Give the extent of all Plasmodium falciparum-infected red blood cells.
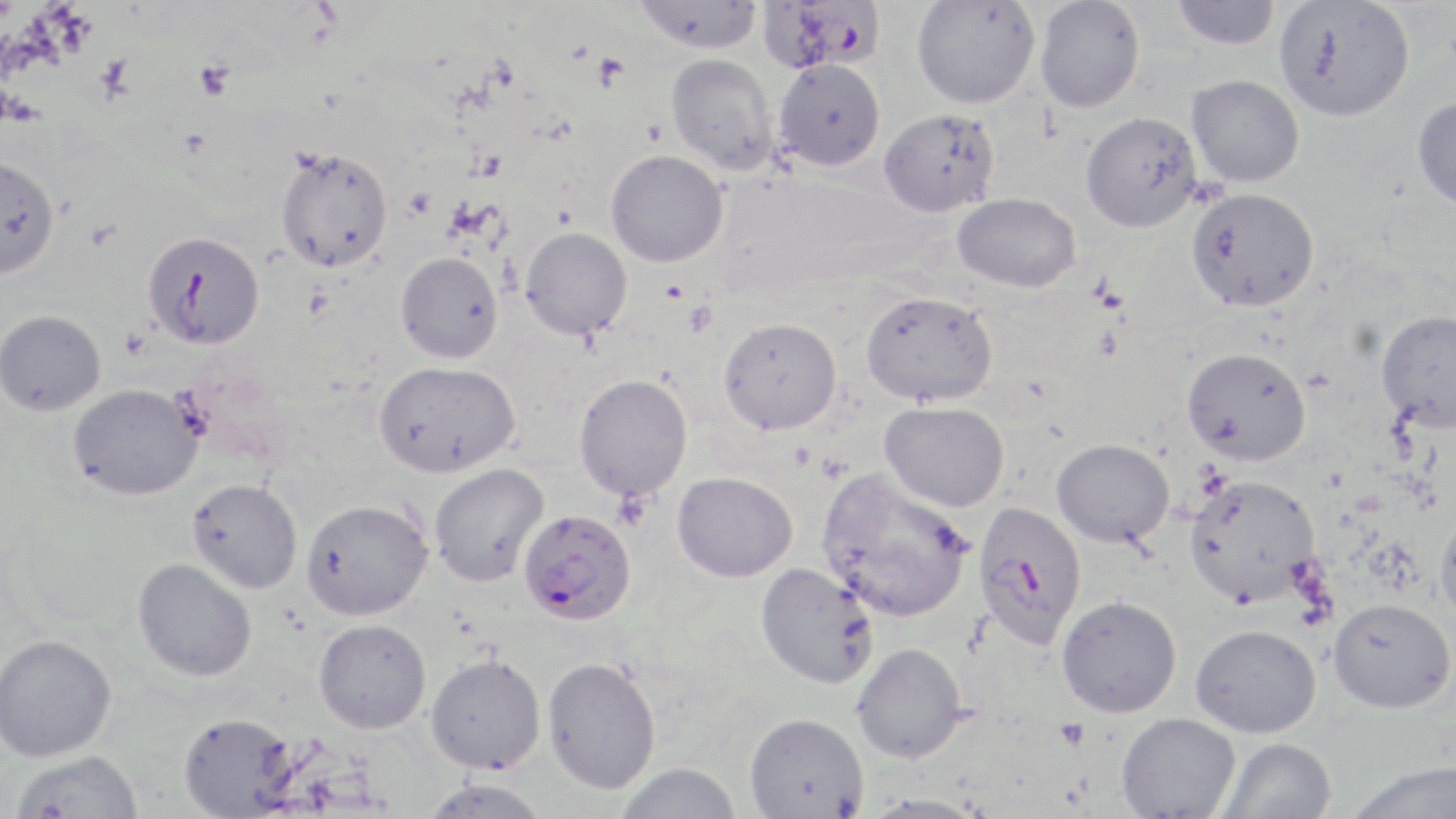
Approximate bounding boxes as [x1, y1, x2, y2] in pixels.
Plasmodium falciparum-infected red blood cells: [758, 0, 885, 74], [142, 230, 265, 349], [973, 501, 1088, 650], [518, 509, 636, 626].

Uninfected red blood cell locations: [632, 0, 765, 54], [911, 0, 1040, 109], [1035, 0, 1145, 113], [1172, 0, 1282, 50], [1274, 0, 1416, 121], [666, 53, 778, 174], [773, 59, 885, 171], [1187, 75, 1304, 188], [1412, 96, 1456, 211], [878, 109, 1000, 217], [1080, 111, 1202, 232], [275, 146, 394, 272], [605, 149, 728, 267], [0, 154, 59, 278], [1186, 187, 1319, 311], [952, 193, 1080, 292], [520, 227, 633, 340], [396, 252, 503, 364], [861, 290, 997, 407], [1375, 308, 1456, 434], [0, 310, 105, 415], [718, 317, 842, 435], [1182, 346, 1312, 465], [374, 360, 519, 478], [573, 374, 692, 501], [67, 383, 203, 500], [879, 401, 1009, 512], [1052, 438, 1174, 547], [429, 463, 549, 587], [817, 469, 974, 622], [672, 471, 797, 582], [1183, 473, 1321, 608], [187, 478, 303, 593], [300, 498, 433, 621], [1434, 507, 1456, 626], [133, 558, 257, 681], [755, 562, 879, 689], [1056, 595, 1182, 717], [1328, 598, 1455, 713], [314, 619, 431, 734], [1190, 624, 1321, 737], [0, 634, 116, 761], [852, 642, 967, 763], [425, 653, 546, 774], [542, 656, 661, 794], [178, 712, 297, 817], [744, 712, 868, 818], [1116, 712, 1241, 818], [1217, 737, 1337, 819], [11, 750, 143, 818], [1344, 760, 1456, 819], [614, 762, 742, 819], [420, 777, 553, 819], [858, 794, 991, 819]. Platelet locations: [592, 52, 631, 91], [195, 60, 236, 101], [1055, 718, 1090, 751]. Slide-level diagnosis: Plasmodium falciparum. Image is 1456×819 pixels. 1000x magnification. One field of a larger specimen. Optical microscopy. May-Grünwald-Giemsa stain. Thin blood film.